Describe the morphology of the red blood cells.
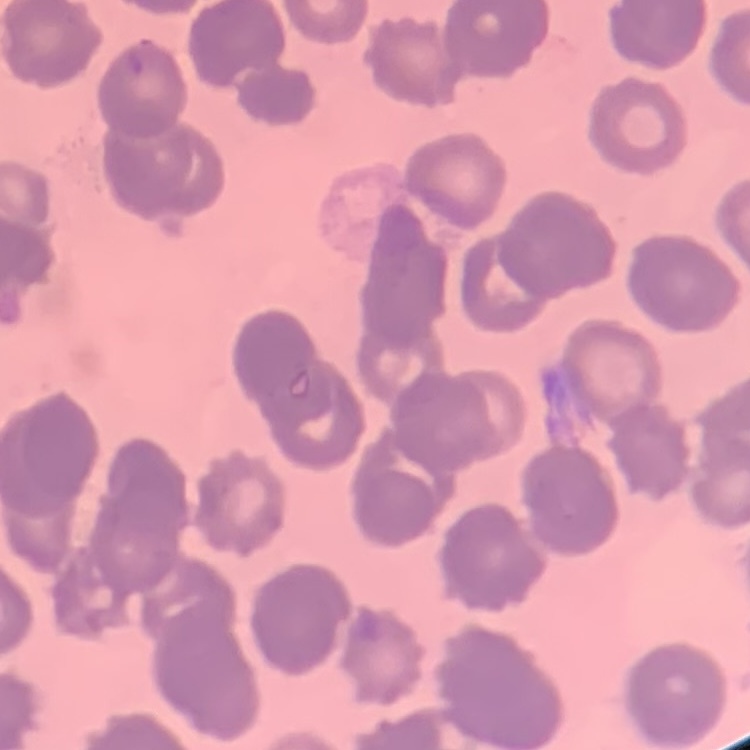

Rouleaux formation.

preparation: thin blood film
stain: Field's or Giemsa
image_type: one tile cut from a larger photomicrograph